Locate every Plasmodium falciparum parasite and give its life-cycle stage, and locate every leukocyte and any debris.
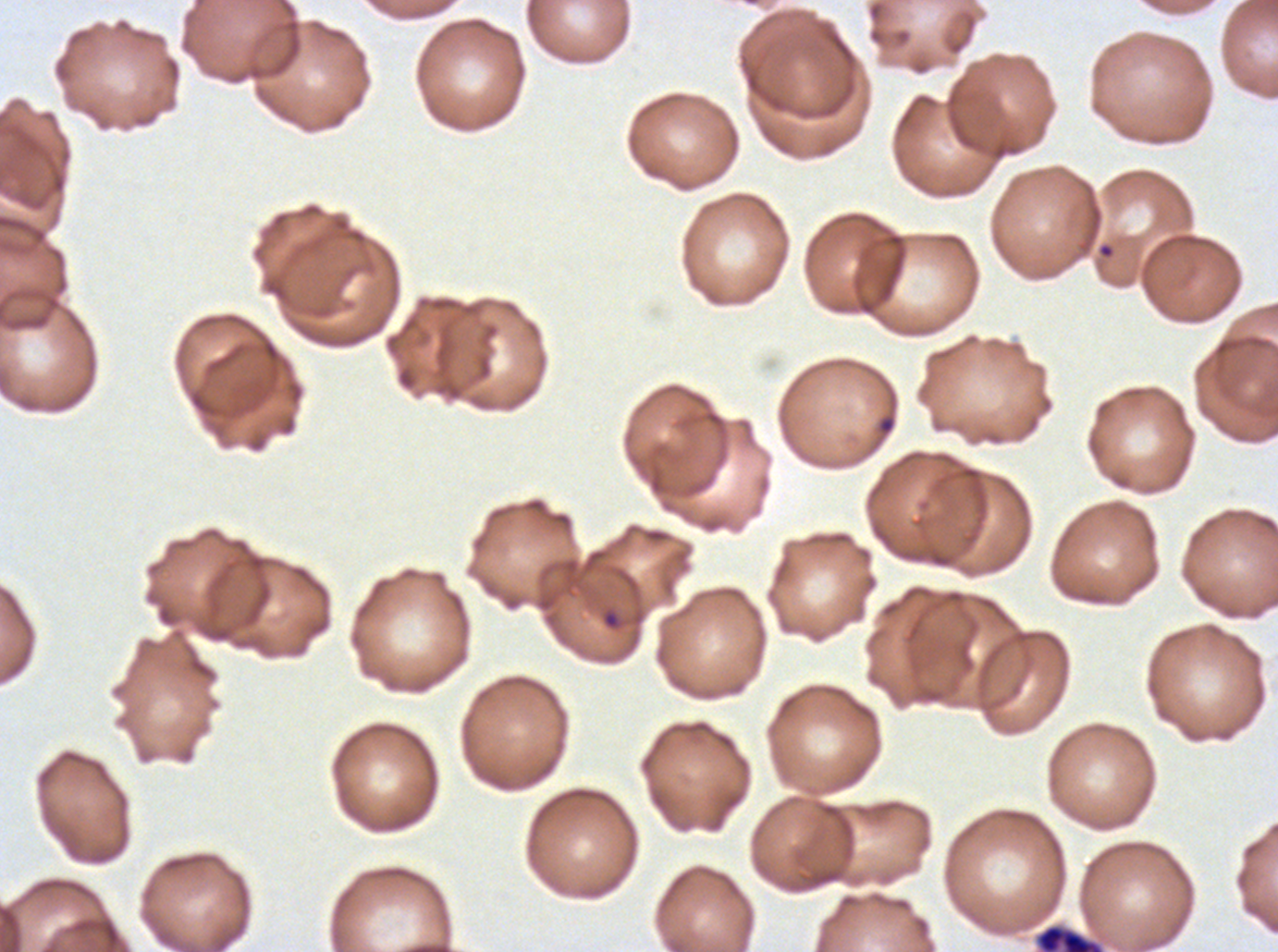

Approximate bounding boxes as (x1, y1, x2, y2) in pixels.
Rings: (600, 605, 625, 631).
Late schizonts: (1034, 922, 1105, 951).
No late-ring/early-trophozoite forms, mid trophozoites, late trophozoites, early schizonts, segmenters, gametocytes, leukocytes, or debris observed.

preparation = thin blood smear
specimen = ex-vivo Plasmodium falciparum culture from a patient in The Gambia, grown for 24 to 48 hours
image size = 1278×952 pixels
life-cycle stages observed = ring, late schizont
stain = Giemsa
field of view = one sub-image of a larger composite